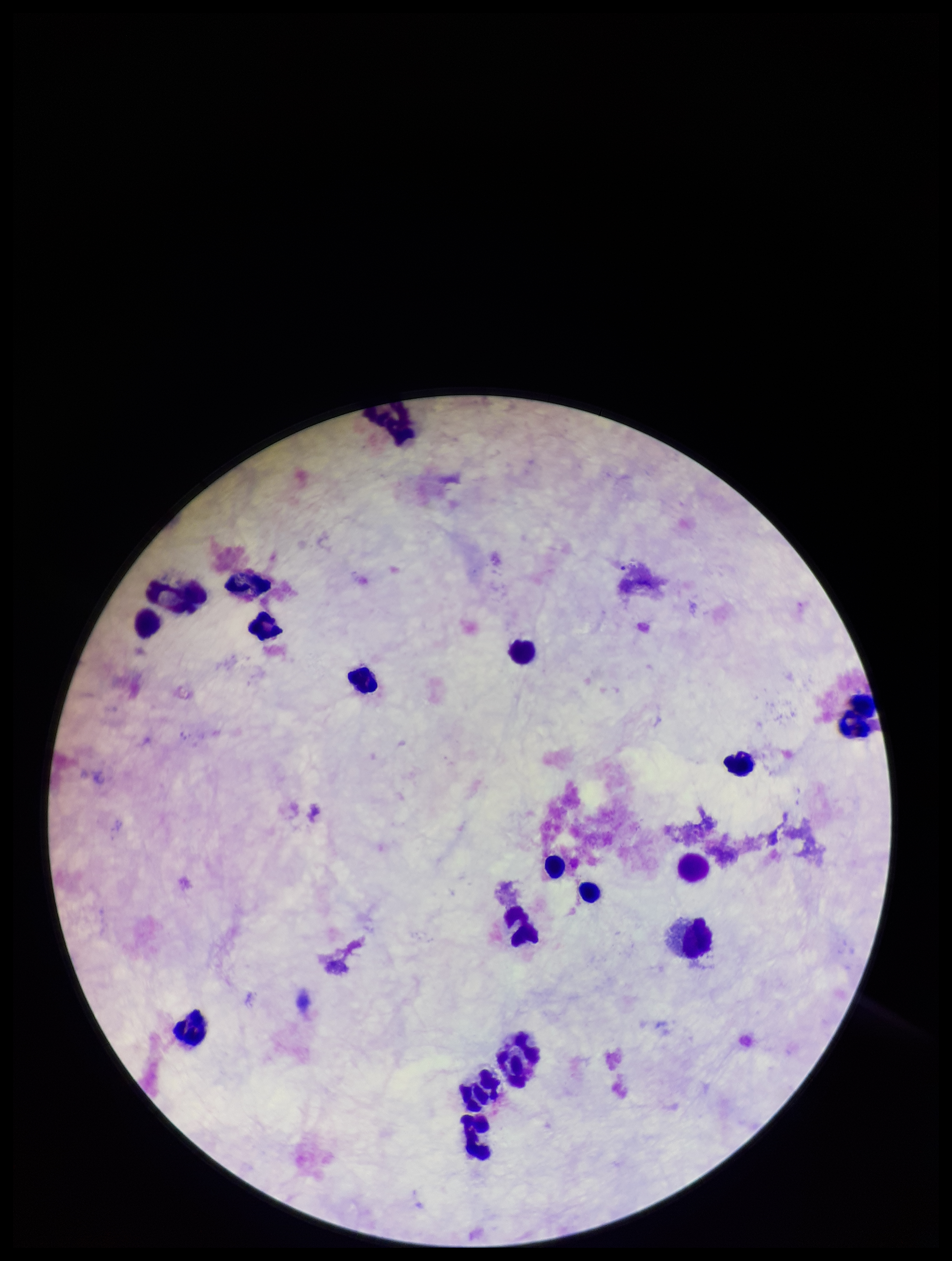

parasite count = 0
preparation = thick blood smear
field of view = one from this slide
Plasmodium parasites = none detected
leukocyte count = 16
image size = 952×1261 pixels
stain = Giemsa
patient malaria status = negative
capture = smartphone photograph through the microscope eyepiece